Outline platelets.
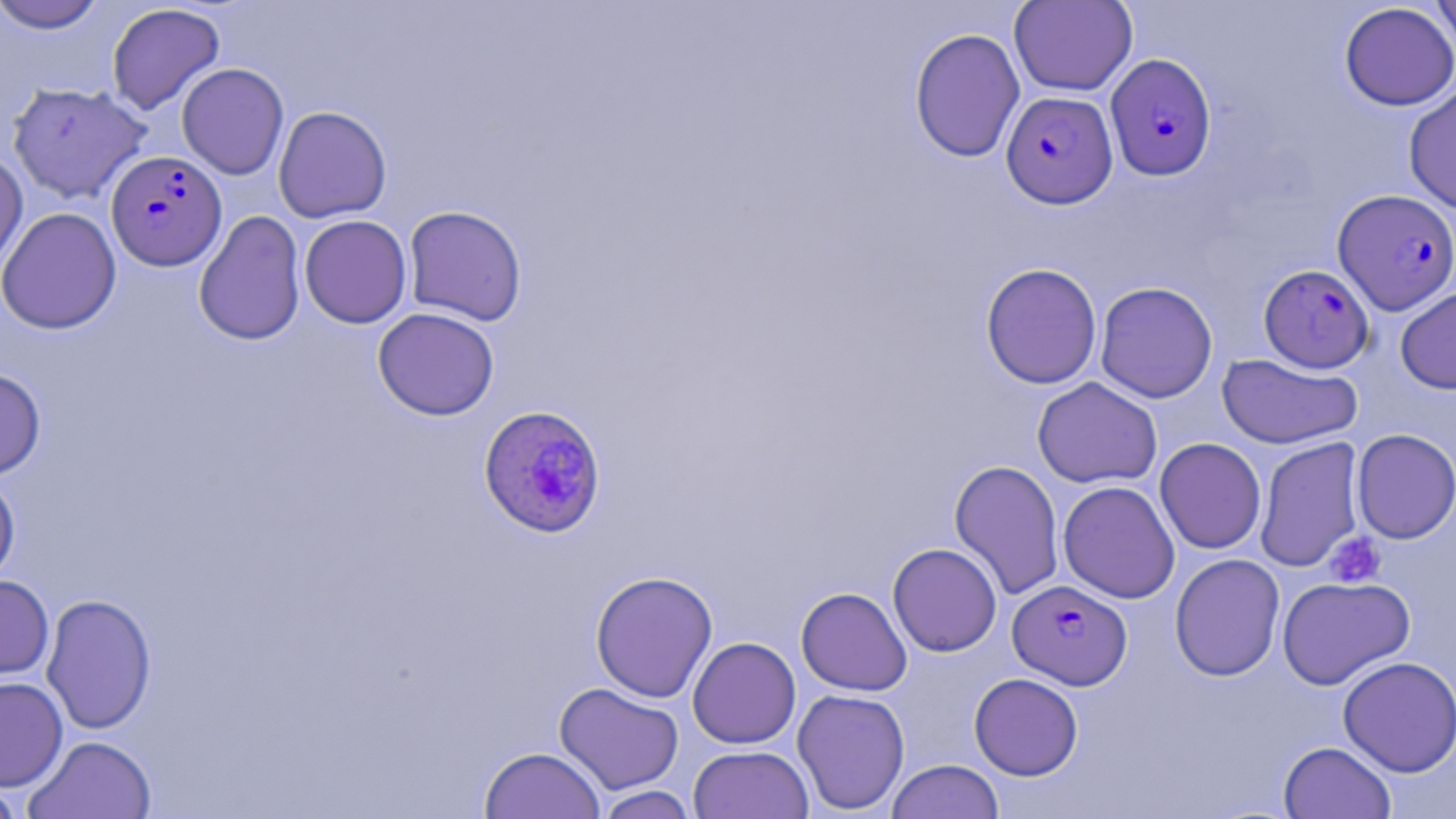
Approximate bounding boxes as [x1, y1, x2, y2] in pixels.
Platelets: [1325, 532, 1386, 588].

Plasmodium falciparum-infected red blood cell locations: [1105, 53, 1217, 181], [1001, 90, 1118, 208], [105, 150, 227, 270], [1333, 189, 1456, 315], [1259, 264, 1374, 373], [478, 405, 607, 538], [1008, 579, 1132, 690]. Uninfected red blood cell locations: [1009, 0, 1137, 96], [1430, 0, 1456, 59], [1, 1, 108, 33], [106, 3, 226, 115], [1339, 3, 1456, 111], [909, 27, 1026, 163], [177, 63, 289, 180], [6, 81, 152, 204], [1404, 83, 1456, 214], [273, 106, 392, 223], [0, 148, 28, 277], [403, 205, 527, 326], [0, 207, 123, 334], [193, 210, 306, 346], [299, 215, 412, 328], [980, 262, 1102, 389], [1095, 281, 1218, 403], [1395, 285, 1456, 394], [373, 307, 500, 421], [1216, 354, 1364, 449], [0, 367, 46, 479], [1032, 376, 1162, 489], [1351, 428, 1456, 544], [1254, 436, 1365, 573], [1154, 437, 1266, 554], [949, 459, 1065, 601], [0, 471, 21, 587], [1058, 480, 1180, 603], [887, 542, 1002, 657], [1169, 553, 1285, 682], [590, 570, 718, 703], [0, 574, 54, 683], [1277, 576, 1415, 690], [796, 587, 912, 696], [41, 593, 157, 735], [687, 636, 801, 749], [1338, 656, 1456, 777], [969, 673, 1083, 780], [0, 675, 68, 792], [554, 682, 684, 795], [792, 688, 911, 815], [23, 734, 157, 819], [1278, 741, 1396, 819], [688, 745, 814, 819], [480, 746, 605, 819], [886, 759, 1004, 819], [0, 777, 27, 819], [594, 785, 698, 819]. Slide-level diagnosis: Plasmodium falciparum. Single field of view. May-Grünwald-Giemsa stain. Image is 1456×819 pixels. Thin blood film. Optical microscopy. 1000x magnification.